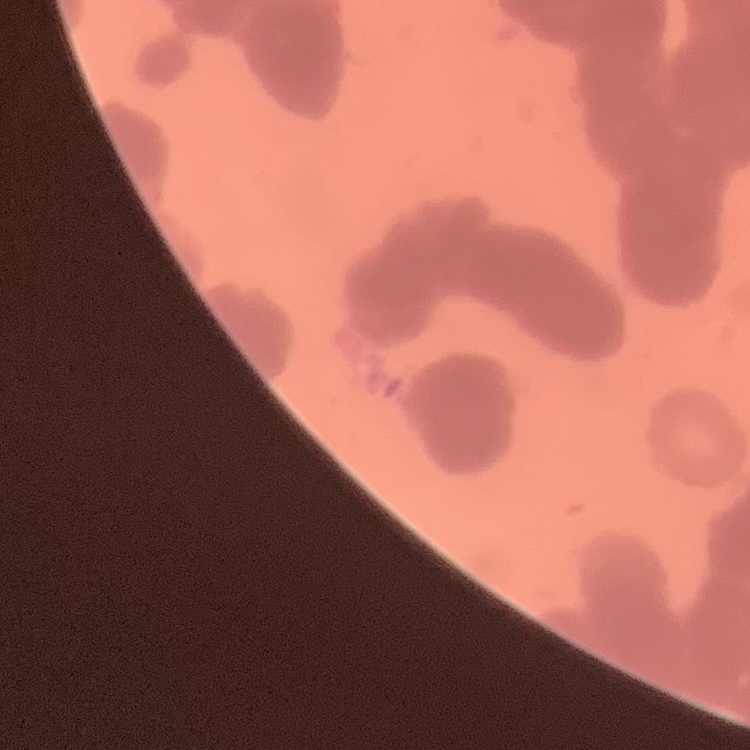

Summary:
  - Erythrocyte morphology: rouleaux formation
  - Stain: Field's or Giemsa
  - Image type: one tile cut from a larger photomicrograph
  - Preparation: thin peripheral smear